State the blood parasite species.
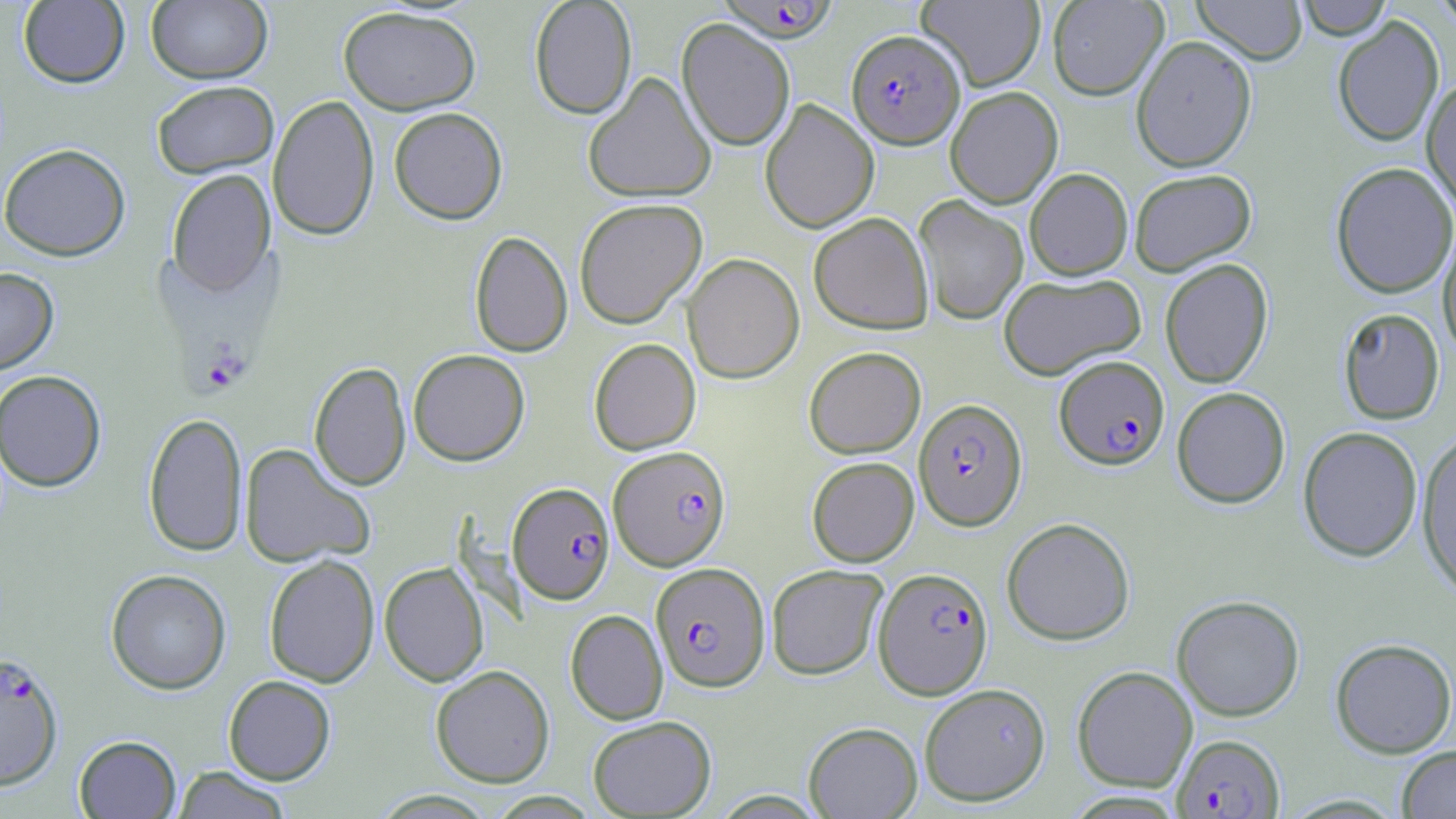

Plasmodium falciparum.

Summary:
  - Coordinate format: approximate bounding boxes as (x1, y1, x2, y2) in pixels
  - Plasmodium falciparum-infected red blood cell locations: (713, 0, 841, 43), (847, 29, 965, 148), (1054, 355, 1169, 469), (913, 398, 1027, 530), (608, 445, 730, 570), (507, 482, 615, 604), (651, 562, 770, 691), (874, 567, 993, 699), (0, 650, 65, 791), (1172, 733, 1285, 818)
  - Uninfected red blood cell locations: (18, 0, 130, 88), (146, 0, 272, 84), (529, 0, 637, 119), (916, 0, 1045, 92), (1047, 0, 1167, 100), (1191, 0, 1308, 64), (1295, 0, 1393, 39), (1431, 0, 1456, 30), (338, 5, 481, 114), (1333, 15, 1444, 147), (677, 18, 795, 151), (1132, 35, 1257, 172), (583, 71, 716, 204), (1421, 77, 1456, 216), (151, 80, 279, 178), (945, 86, 1063, 208), (269, 95, 379, 241), (760, 98, 879, 233), (389, 107, 508, 224), (0, 143, 130, 261), (1331, 162, 1456, 298), (1024, 168, 1133, 280), (1129, 168, 1257, 275), (166, 169, 276, 296), (914, 195, 1029, 325), (574, 197, 707, 329), (808, 212, 933, 333), (1438, 225, 1456, 359), (469, 230, 572, 358), (682, 253, 804, 384), (1160, 258, 1273, 388), (0, 267, 58, 375), (998, 272, 1146, 380), (1338, 308, 1444, 424), (589, 338, 701, 455), (804, 346, 926, 458), (408, 348, 530, 466), (309, 361, 411, 491), (0, 370, 107, 491), (1172, 387, 1291, 508), (143, 411, 247, 557), (1298, 426, 1423, 562), (1415, 430, 1456, 600), (239, 443, 376, 568), (807, 456, 919, 567), (1001, 517, 1135, 645), (264, 554, 380, 688), (379, 561, 489, 686), (767, 564, 888, 680), (105, 569, 232, 695), (1171, 595, 1304, 721), (565, 609, 668, 725), (1330, 638, 1456, 758), (430, 664, 555, 787), (1072, 666, 1198, 792), (223, 675, 335, 784), (919, 682, 1051, 806), (588, 715, 716, 818), (803, 721, 923, 818), (74, 735, 181, 818), (1397, 746, 1456, 818), (170, 766, 293, 819)
  - Modality: optical microscopy
  - Image size: 1456×819 pixels
  - Stain: May-Grünwald-Giemsa
  - Field of view: one of a larger specimen
  - Preparation: thin blood film
  - Magnification: 1000x